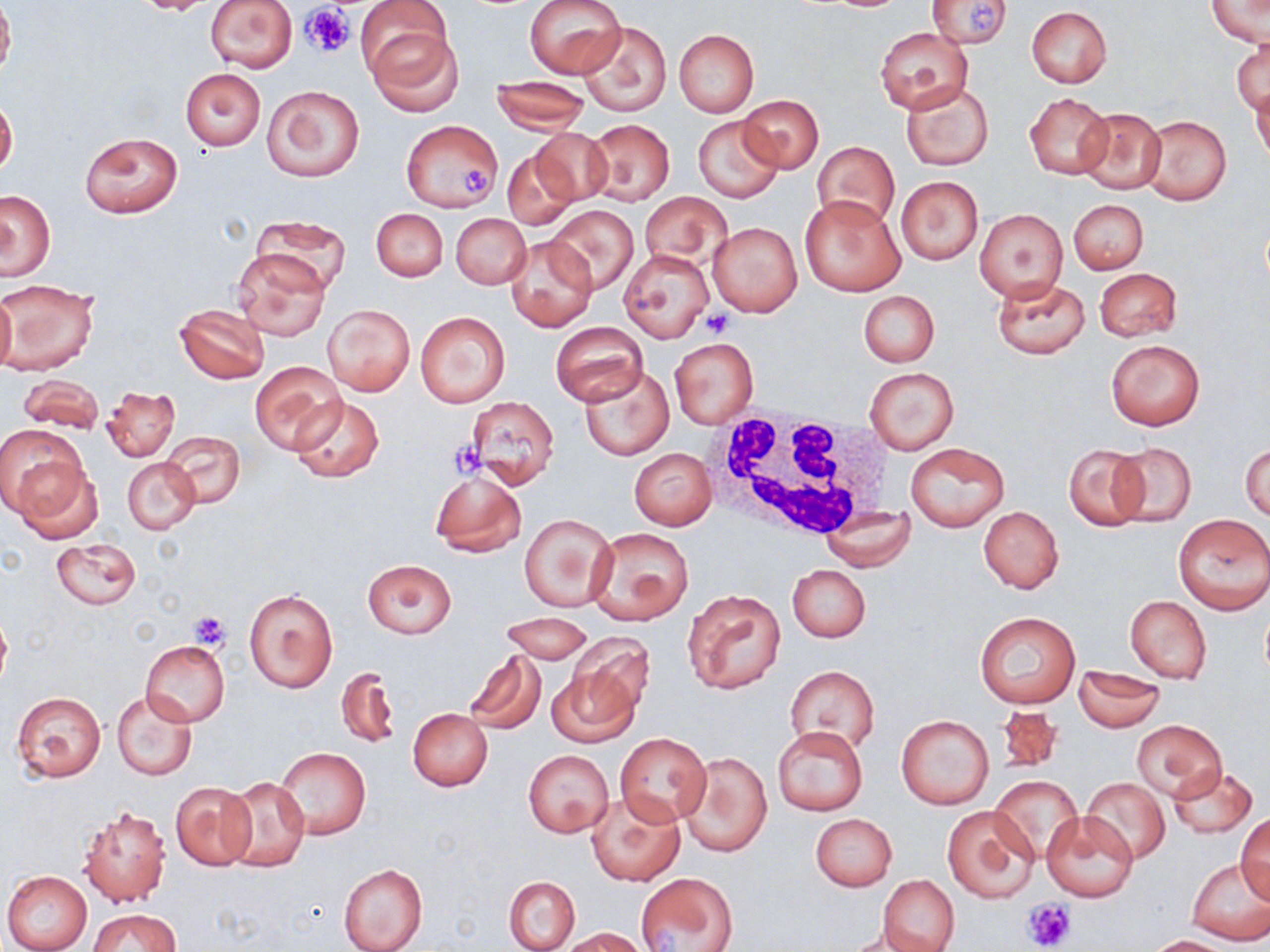

Summary:
  - Coordinate format: approximate bounding boxes as named x1/y1/x2/y2 corners in pixels
  - White blood cell locations: (x1=702, y1=410, x2=897, y2=544)
  - Uninfected red blood cell locations: (x1=0, y1=0, x2=14, y2=80), (x1=131, y1=0, x2=226, y2=16), (x1=204, y1=0, x2=298, y2=72), (x1=526, y1=0, x2=627, y2=79), (x1=930, y1=0, x2=1012, y2=51), (x1=1206, y1=0, x2=1269, y2=47), (x1=356, y1=1, x2=455, y2=90), (x1=1025, y1=7, x2=1111, y2=89), (x1=577, y1=21, x2=672, y2=117), (x1=875, y1=25, x2=973, y2=114), (x1=371, y1=27, x2=466, y2=116), (x1=674, y1=30, x2=759, y2=118), (x1=1232, y1=39, x2=1268, y2=116), (x1=180, y1=68, x2=266, y2=150), (x1=492, y1=76, x2=590, y2=134), (x1=899, y1=81, x2=994, y2=171), (x1=261, y1=85, x2=363, y2=181), (x1=1252, y1=85, x2=1270, y2=167), (x1=1025, y1=93, x2=1111, y2=179), (x1=738, y1=94, x2=823, y2=174), (x1=0, y1=97, x2=18, y2=177), (x1=1076, y1=107, x2=1166, y2=194), (x1=1140, y1=114, x2=1232, y2=205), (x1=693, y1=115, x2=783, y2=202), (x1=582, y1=119, x2=675, y2=205), (x1=400, y1=120, x2=504, y2=212), (x1=528, y1=127, x2=613, y2=207), (x1=80, y1=132, x2=183, y2=218), (x1=813, y1=143, x2=900, y2=230), (x1=501, y1=148, x2=579, y2=230), (x1=896, y1=176, x2=983, y2=264), (x1=1, y1=191, x2=56, y2=279), (x1=638, y1=191, x2=732, y2=270), (x1=799, y1=194, x2=905, y2=296), (x1=1069, y1=199, x2=1148, y2=274), (x1=545, y1=204, x2=639, y2=294), (x1=372, y1=208, x2=448, y2=281), (x1=975, y1=209, x2=1067, y2=300), (x1=450, y1=213, x2=530, y2=289), (x1=250, y1=215, x2=351, y2=292), (x1=708, y1=221, x2=803, y2=318), (x1=506, y1=234, x2=596, y2=331), (x1=232, y1=248, x2=330, y2=341), (x1=618, y1=248, x2=713, y2=343), (x1=1095, y1=267, x2=1182, y2=342), (x1=991, y1=276, x2=1089, y2=359), (x1=1, y1=281, x2=99, y2=375), (x1=0, y1=290, x2=15, y2=375), (x1=858, y1=290, x2=939, y2=367), (x1=324, y1=304, x2=414, y2=395), (x1=174, y1=305, x2=269, y2=384), (x1=415, y1=311, x2=510, y2=408), (x1=551, y1=321, x2=647, y2=406), (x1=670, y1=338, x2=758, y2=428), (x1=1106, y1=339, x2=1204, y2=430), (x1=251, y1=361, x2=344, y2=455), (x1=578, y1=366, x2=674, y2=460), (x1=863, y1=367, x2=960, y2=454), (x1=17, y1=374, x2=106, y2=435), (x1=102, y1=388, x2=179, y2=462), (x1=290, y1=394, x2=385, y2=484), (x1=464, y1=397, x2=559, y2=488), (x1=0, y1=426, x2=85, y2=519), (x1=162, y1=431, x2=244, y2=509), (x1=1108, y1=441, x2=1198, y2=526), (x1=1240, y1=441, x2=1269, y2=523), (x1=906, y1=442, x2=1009, y2=531), (x1=1064, y1=444, x2=1149, y2=531), (x1=629, y1=448, x2=718, y2=530), (x1=10, y1=457, x2=101, y2=543), (x1=123, y1=458, x2=198, y2=534), (x1=429, y1=469, x2=527, y2=558), (x1=820, y1=505, x2=914, y2=571), (x1=978, y1=506, x2=1064, y2=593), (x1=518, y1=512, x2=618, y2=612), (x1=1173, y1=514, x2=1270, y2=614), (x1=586, y1=525, x2=694, y2=625), (x1=52, y1=537, x2=139, y2=609), (x1=361, y1=559, x2=457, y2=639), (x1=787, y1=565, x2=870, y2=643), (x1=681, y1=588, x2=787, y2=695), (x1=245, y1=589, x2=337, y2=694), (x1=1125, y1=596, x2=1212, y2=682), (x1=0, y1=608, x2=11, y2=694), (x1=501, y1=611, x2=593, y2=664), (x1=973, y1=612, x2=1079, y2=709), (x1=567, y1=635, x2=655, y2=719), (x1=141, y1=641, x2=230, y2=727), (x1=460, y1=650, x2=547, y2=736), (x1=784, y1=665, x2=881, y2=759), (x1=335, y1=666, x2=399, y2=751), (x1=546, y1=666, x2=639, y2=748), (x1=1073, y1=667, x2=1165, y2=731), (x1=112, y1=689, x2=197, y2=781), (x1=11, y1=690, x2=107, y2=782), (x1=996, y1=702, x2=1068, y2=774), (x1=408, y1=708, x2=493, y2=791), (x1=896, y1=714, x2=994, y2=809), (x1=1133, y1=721, x2=1225, y2=800), (x1=772, y1=724, x2=868, y2=817), (x1=616, y1=733, x2=710, y2=826), (x1=277, y1=747, x2=370, y2=838), (x1=523, y1=749, x2=614, y2=838), (x1=678, y1=752, x2=772, y2=858), (x1=1166, y1=764, x2=1258, y2=838), (x1=223, y1=776, x2=310, y2=871), (x1=989, y1=776, x2=1084, y2=865), (x1=1081, y1=777, x2=1171, y2=865), (x1=169, y1=782, x2=257, y2=872), (x1=586, y1=792, x2=684, y2=886), (x1=79, y1=804, x2=172, y2=908), (x1=942, y1=804, x2=1038, y2=904), (x1=810, y1=812, x2=896, y2=892), (x1=1042, y1=812, x2=1138, y2=901), (x1=1237, y1=812, x2=1269, y2=902), (x1=1186, y1=858, x2=1270, y2=945), (x1=338, y1=863, x2=427, y2=952), (x1=1, y1=870, x2=93, y2=952), (x1=635, y1=870, x2=738, y2=951), (x1=877, y1=875, x2=960, y2=952), (x1=504, y1=876, x2=579, y2=951), (x1=90, y1=909, x2=178, y2=952), (x1=562, y1=928, x2=649, y2=952), (x1=1148, y1=935, x2=1237, y2=952)
  - Platelet locations: (x1=970, y1=1, x2=998, y2=35), (x1=305, y1=4, x2=353, y2=55), (x1=458, y1=165, x2=490, y2=198), (x1=701, y1=308, x2=732, y2=337), (x1=448, y1=440, x2=484, y2=475), (x1=187, y1=610, x2=231, y2=649), (x1=1023, y1=897, x2=1077, y2=950)
  - Slide-level diagnosis: negative for blood parasites
  - Image size: 1270×952 pixels
  - Modality: optical microscopy
  - Field of view: one of a larger specimen
  - Magnification: 1000x
  - Preparation: thin blood smear
  - Stain: May-Grünwald-Giemsa